State the preparation type.
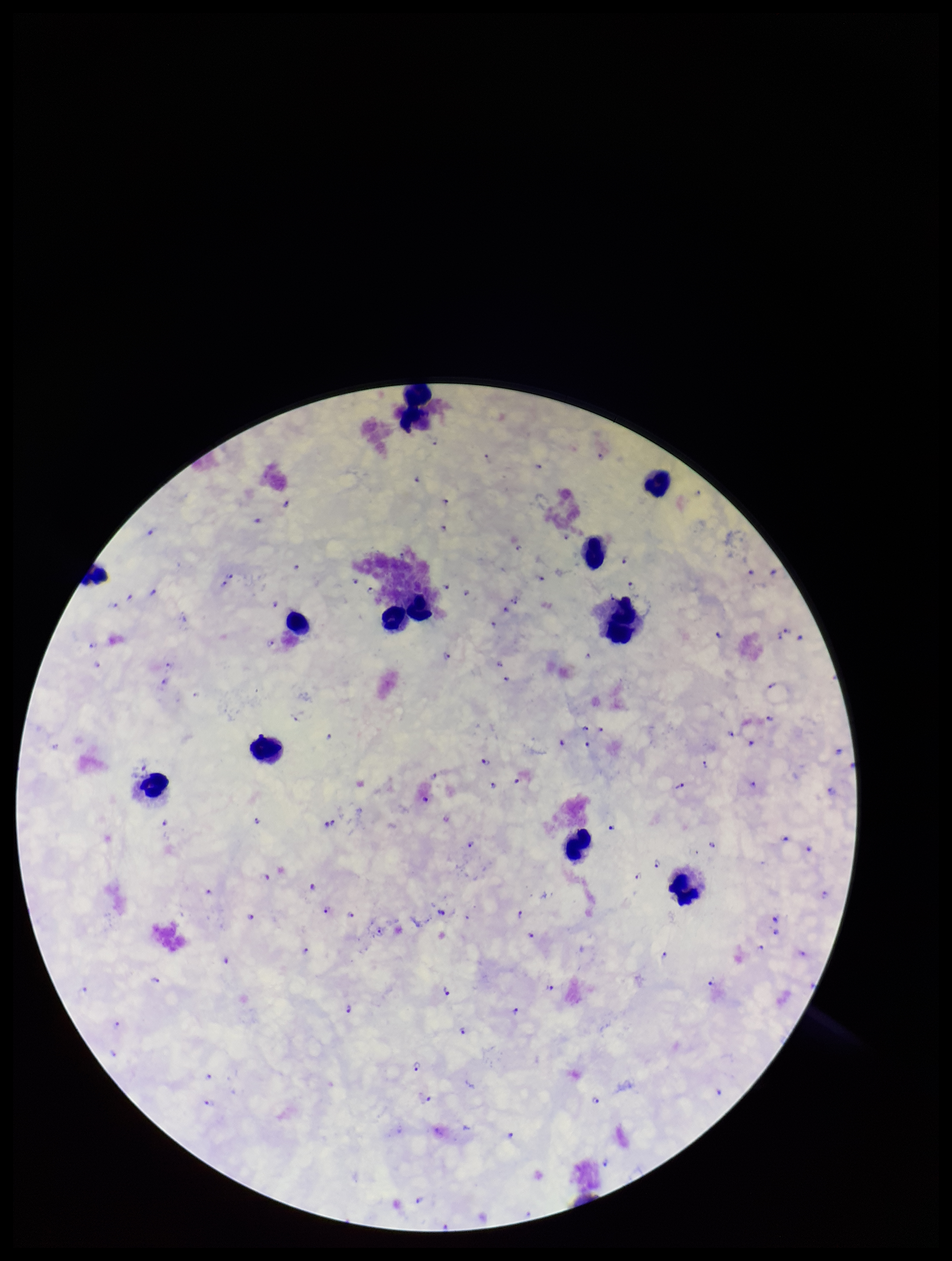
Thick.

stain = Giemsa
leukocyte count = 12
capture = smartphone photograph through the microscope eyepiece
species reported for this patient = Plasmodium falciparum
Plasmodium parasites = detected
parasite count = 115
field of view = single
image size = 952×1261 pixels
patient malaria status = positive